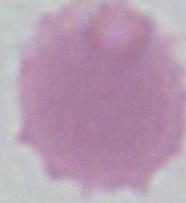
{
  "magnification": "1000x",
  "identification": "erythrocyte",
  "modality": "photomicrograph"
}